Describe the morphology of the erythrocytes.
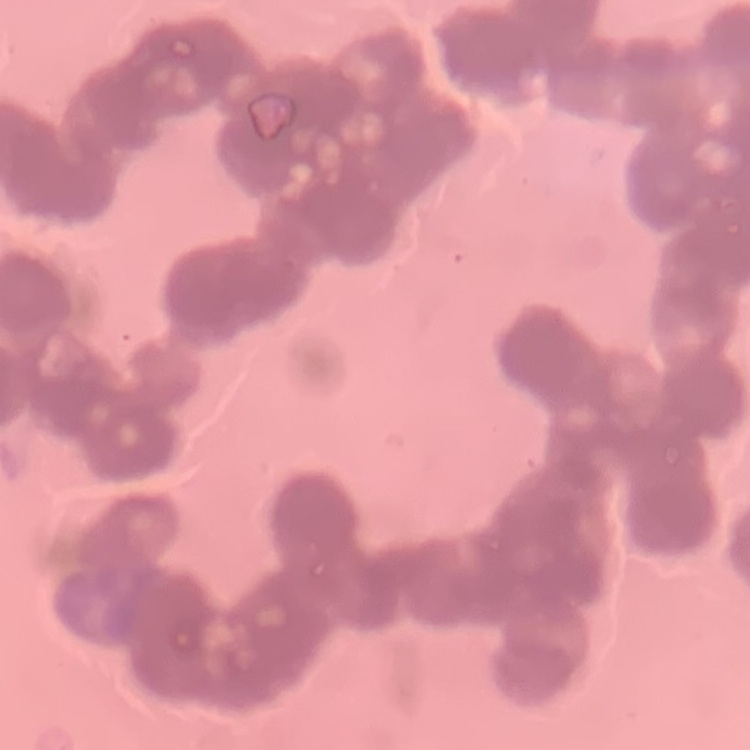
They show rouleaux formation.

Field's or Giemsa stain. Square crop of a larger photomicrograph. Thin blood film.